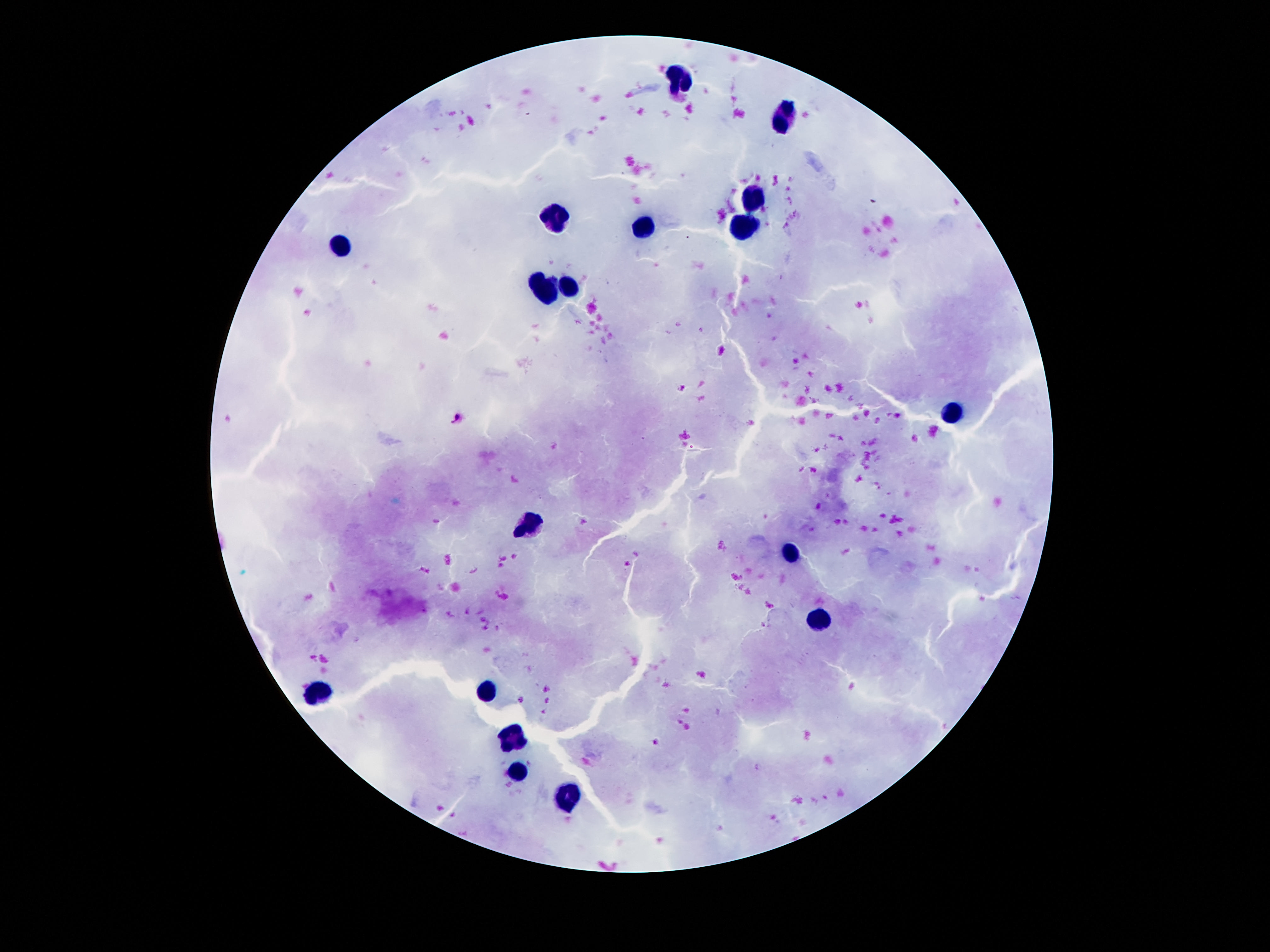

{
  "image_size": "1270×952 pixels",
  "patient_malaria_status": "uninfected",
  "capture": "smartphone camera through the microscope eyepiece",
  "field_of_view": "one from this slide",
  "magnification": "100x",
  "stain": "Giemsa",
  "leukocyte_locations": "approximate centers as {x, y} in pixels: {675, 78}, {786, 118}, {752, 198}, {553, 216}, {641, 224}, {744, 226}, {341, 245}, {545, 285}, {568, 286}, {956, 413}, {526, 527}, {790, 556}, {817, 621}, {320, 689}, {490, 689}, {511, 741}, {517, 774}, {565, 798}",
  "preparation": "thick blood smear"
}